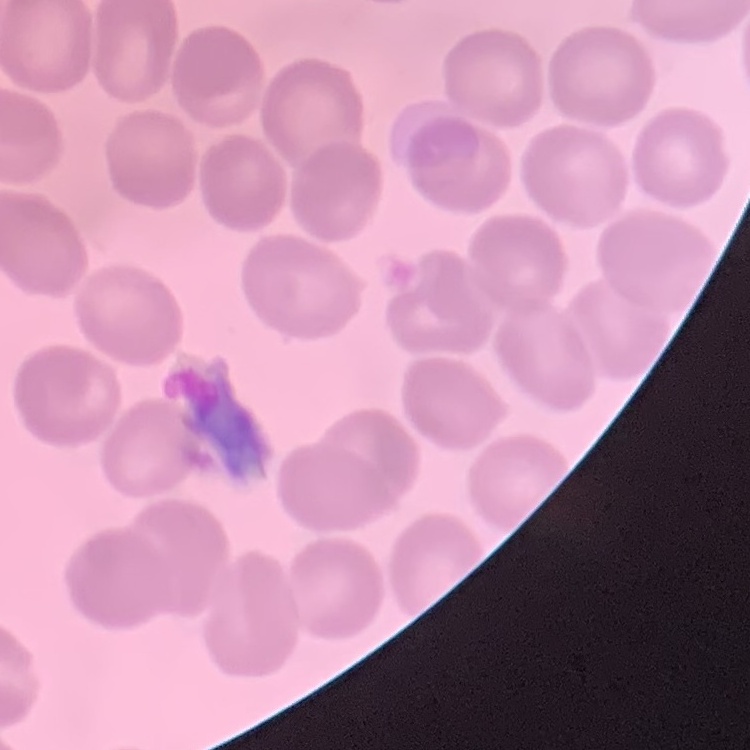

Summary:
  - Red blood cell morphology: no rouleaux formation
  - Preparation: thin blood smear
  - Image type: square crop of a larger photomicrograph
  - Stain: Field's or Giemsa